Report the malaria status of this cell.
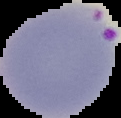
Parasitized.

From a thin blood film. Image is 121×118 pixels. The area outside the segmented cell region is set to black.